Locate every Plasmodium ovale-infected red blood cell.
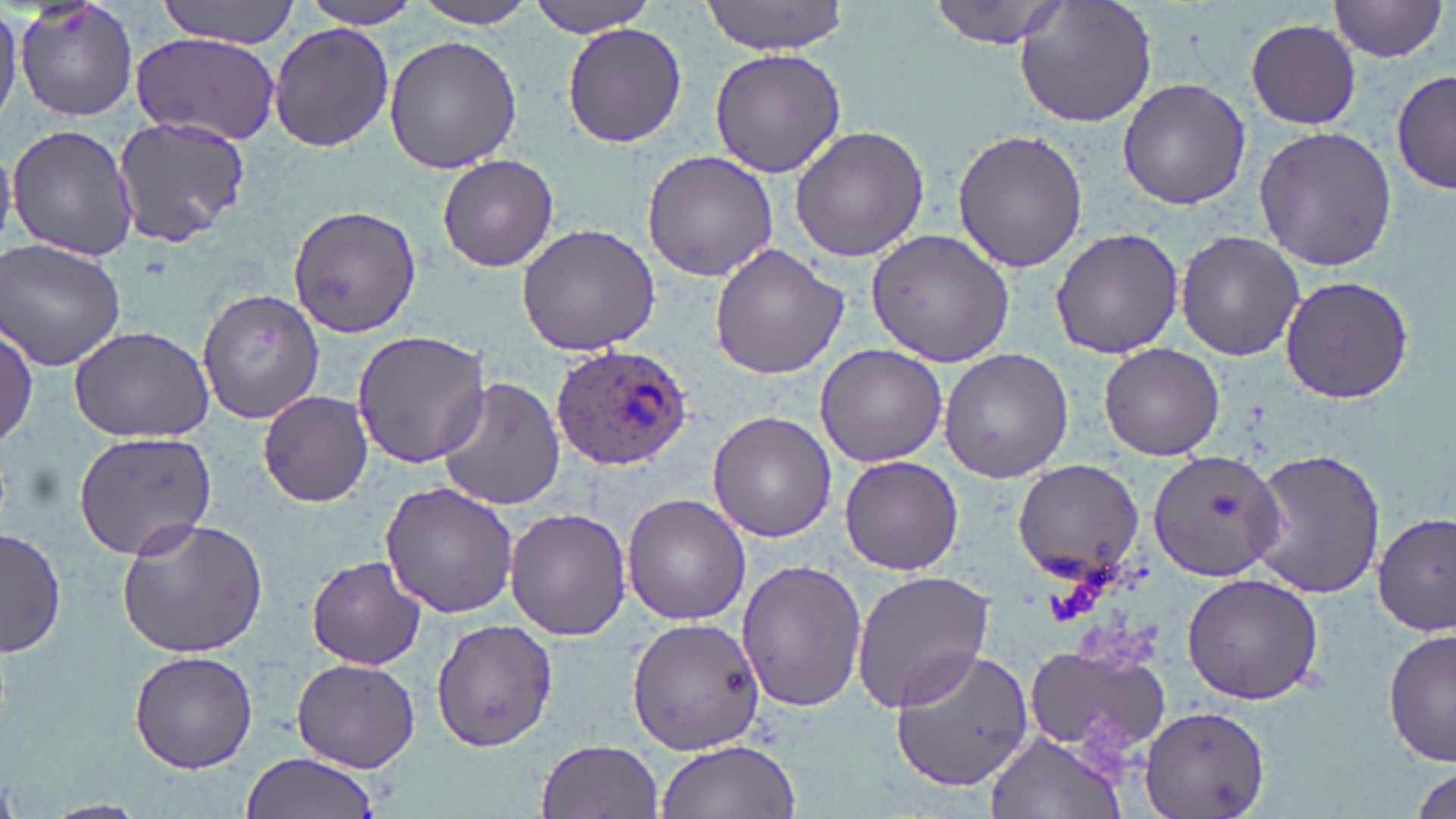

Approximate bounding boxes as named x1/y1/x2/y2 corners in pixels.
Plasmodium ovale-infected red blood cells: (x1=551, y1=346, x2=695, y2=471).

slide-level diagnosis = Plasmodium ovale
magnification = 1000x
image size = 1456×819 pixels
field of view = single
stain = May-Grünwald-Giemsa
modality = optical microscopy
preparation = thin blood smear
uninfected red blood cell locations = approximate bounding boxes as named x1/y1/x2/y2 corners in pixels: (x1=0, y1=0, x2=21, y2=127), (x1=15, y1=0, x2=139, y2=122), (x1=153, y1=0, x2=301, y2=45), (x1=529, y1=0, x2=658, y2=37), (x1=698, y1=0, x2=855, y2=55), (x1=930, y1=0, x2=1069, y2=49), (x1=1014, y1=0, x2=1155, y2=129), (x1=296, y1=1, x2=425, y2=28), (x1=408, y1=1, x2=541, y2=28), (x1=1329, y1=1, x2=1451, y2=65), (x1=1243, y1=18, x2=1363, y2=129), (x1=268, y1=22, x2=394, y2=154), (x1=562, y1=22, x2=686, y2=148), (x1=131, y1=32, x2=281, y2=143), (x1=384, y1=34, x2=521, y2=175), (x1=709, y1=48, x2=846, y2=176), (x1=1391, y1=67, x2=1456, y2=198), (x1=1117, y1=78, x2=1250, y2=210), (x1=112, y1=115, x2=255, y2=247), (x1=7, y1=124, x2=138, y2=260), (x1=1251, y1=125, x2=1397, y2=272), (x1=789, y1=126, x2=928, y2=263), (x1=952, y1=129, x2=1088, y2=274), (x1=642, y1=149, x2=778, y2=284), (x1=437, y1=154, x2=559, y2=272), (x1=286, y1=204, x2=421, y2=338), (x1=516, y1=222, x2=662, y2=355), (x1=1049, y1=227, x2=1183, y2=358), (x1=865, y1=228, x2=1016, y2=367), (x1=1175, y1=232, x2=1305, y2=360), (x1=1, y1=238, x2=127, y2=372), (x1=709, y1=244, x2=846, y2=379), (x1=1278, y1=276, x2=1414, y2=405), (x1=196, y1=287, x2=327, y2=425), (x1=0, y1=319, x2=38, y2=452), (x1=68, y1=322, x2=215, y2=443), (x1=351, y1=330, x2=492, y2=470), (x1=1099, y1=342, x2=1224, y2=460), (x1=814, y1=344, x2=948, y2=467), (x1=939, y1=350, x2=1073, y2=481), (x1=436, y1=379, x2=564, y2=510), (x1=258, y1=389, x2=373, y2=508), (x1=708, y1=410, x2=838, y2=542), (x1=72, y1=429, x2=218, y2=561), (x1=1244, y1=447, x2=1388, y2=599), (x1=1147, y1=448, x2=1285, y2=579), (x1=839, y1=454, x2=964, y2=574), (x1=1011, y1=460, x2=1143, y2=579), (x1=379, y1=479, x2=520, y2=618), (x1=622, y1=494, x2=750, y2=626), (x1=504, y1=506, x2=631, y2=641), (x1=1374, y1=513, x2=1454, y2=637), (x1=114, y1=515, x2=269, y2=658), (x1=1, y1=526, x2=67, y2=660), (x1=307, y1=555, x2=427, y2=671), (x1=735, y1=558, x2=867, y2=714), (x1=851, y1=570, x2=995, y2=710), (x1=1180, y1=572, x2=1324, y2=705), (x1=627, y1=617, x2=764, y2=757), (x1=430, y1=618, x2=556, y2=752), (x1=1383, y1=627, x2=1455, y2=768), (x1=1021, y1=640, x2=1172, y2=760), (x1=888, y1=642, x2=1036, y2=792), (x1=126, y1=649, x2=260, y2=774), (x1=291, y1=656, x2=423, y2=772), (x1=1139, y1=705, x2=1268, y2=819), (x1=985, y1=732, x2=1126, y2=819), (x1=535, y1=738, x2=664, y2=819), (x1=657, y1=740, x2=800, y2=819), (x1=238, y1=753, x2=380, y2=819), (x1=1410, y1=760, x2=1454, y2=819)